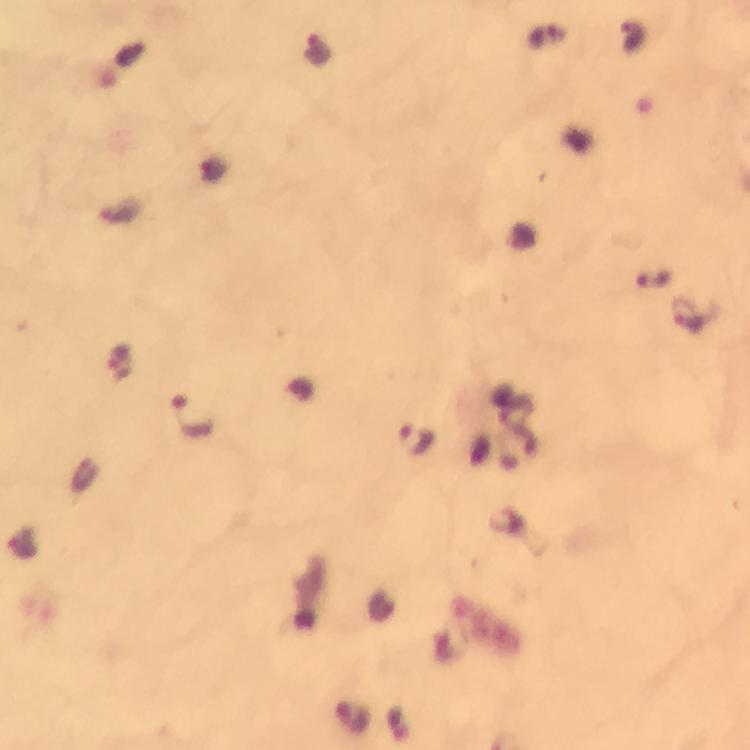
Approximate object centers, in pixels from the top-left corner.
Summary:
  - Plasmodium parasite locations: (x=687, y=315), (x=191, y=415), (x=416, y=439)
  - Preparation: thick smear
  - Magnification: 100x
  - Context: from a diagnostic examination for malaria
  - Immersion oil: applied
  - Image size: 750×750 pixels
  - Cropped from: a single field of view
  - Capture: smartphone mounted on the microscope
  - Stain: Giemsa